Assess the morphology of the red blood cells.
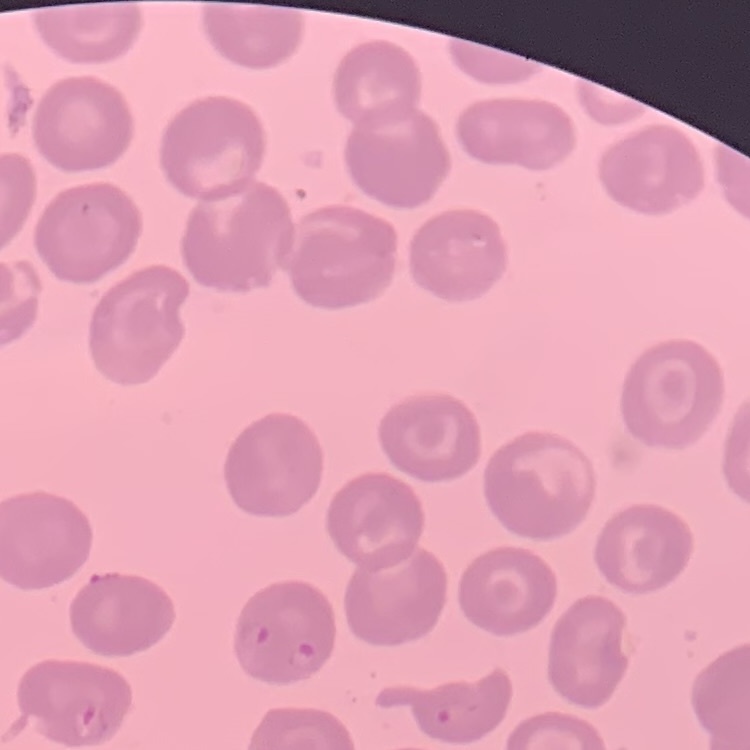
They show no rouleaux formation.

{
  "preparation": "thin blood film",
  "stain": "Field's or Giemsa",
  "image_type": "one tile cut from a larger photomicrograph"
}